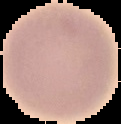
Summary:
  - Result: no Plasmodium parasites detected
  - Image size: 121×124 pixels
  - Preparation: thin blood film
  - Image type: cell region segmented out of the field of view; surrounding area masked to black